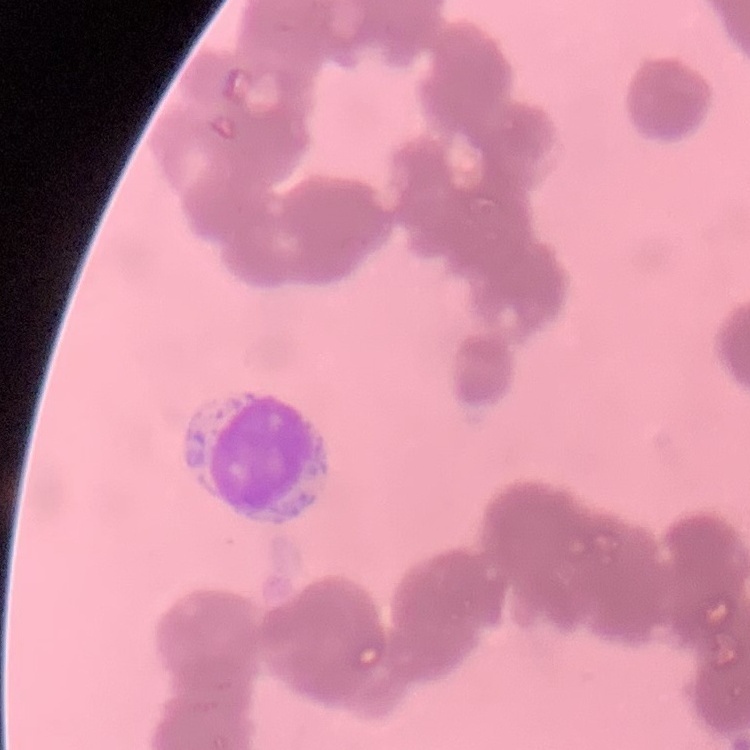 The erythrocytes show rouleaux formation. Square crop of a larger photomicrograph. Thin peripheral smear. Stained with either Field's or Giemsa.